Name the parasite shown.
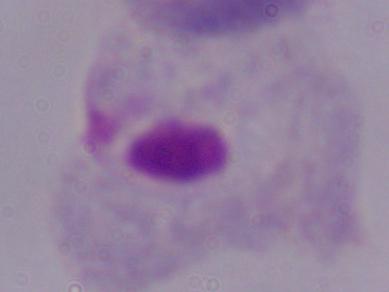
This is a trichomonad.

Summary:
  - Modality: photomicrograph
  - Magnification: 1000x